Point out each malaria parasite.
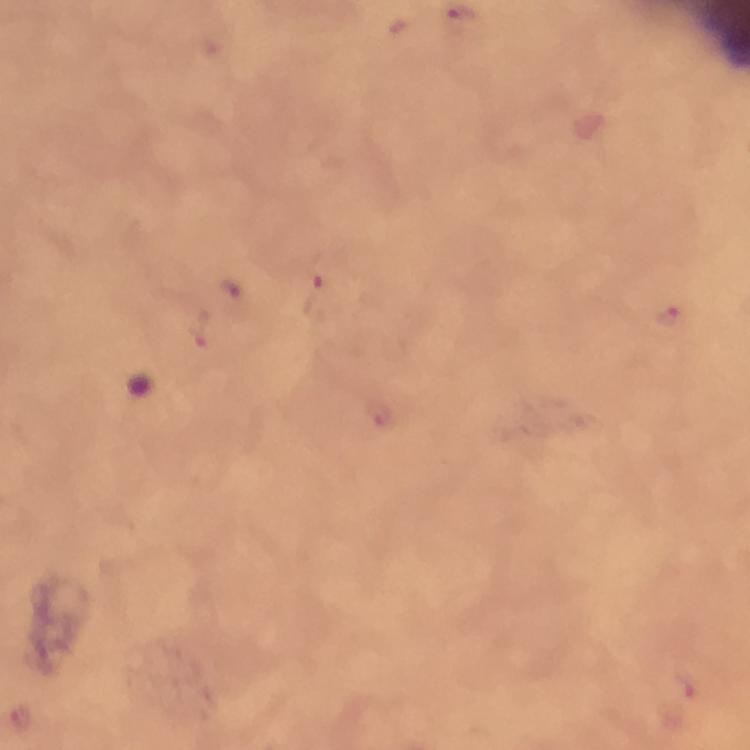
Approximate centers as {x, y} in pixels.
Malaria parasites: {319, 281}, {235, 291}, {671, 314}, {202, 330}, {686, 687}.

magnification = 100x
capture = smartphone photograph through a microscope
image size = 750×750 pixels
preparation = thick blood film
stain = Giemsa
immersion oil = used
cropped from = a single field of view
context = from a diagnostic examination for malaria